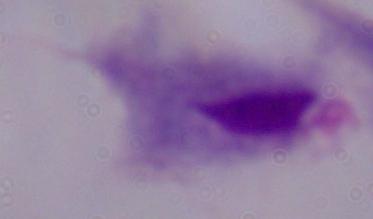

Summary:
  - Identification: trichomonad
  - Magnification: 1000x
  - Modality: micrograph